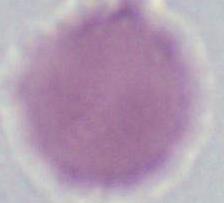
Summary:
  - Magnification: 1000x
  - Identification: erythrocyte
  - Modality: photomicrograph